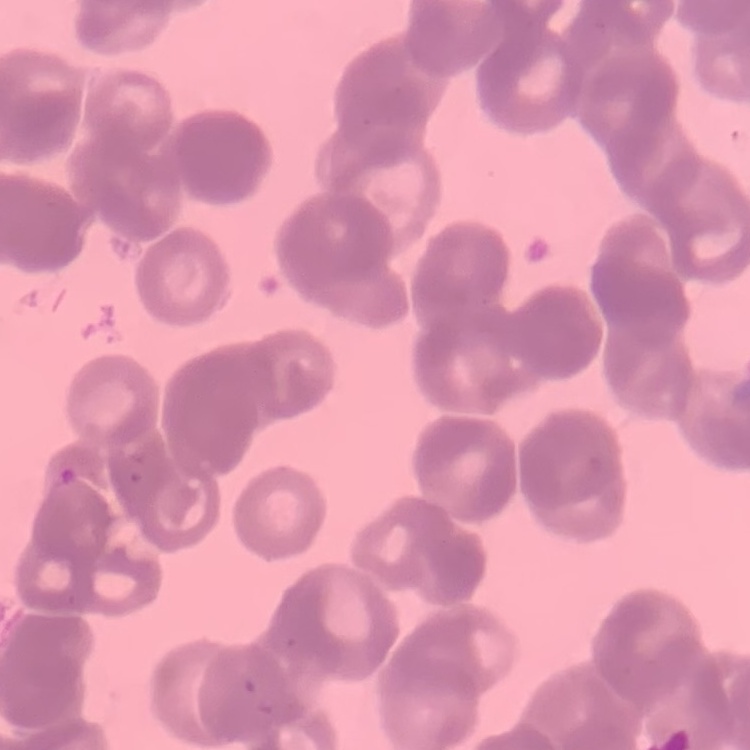

The red blood cells exhibit rouleaux formation. Thin peripheral smear. One tile cut from a larger photomicrograph. Field's or Giemsa stain.